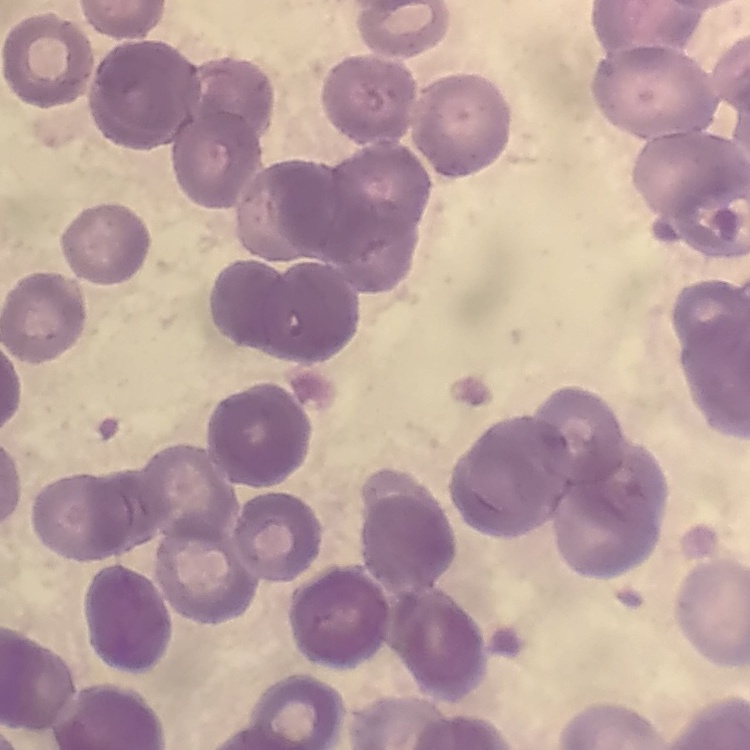

red blood cell morphology = rouleaux formation
image type = square crop of a larger photomicrograph
stain = Field's or Giemsa
preparation = thin blood film